Identify the parasite.
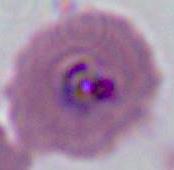
Plasmodium.

modality = photomicrograph
magnification = 400x or 1000x